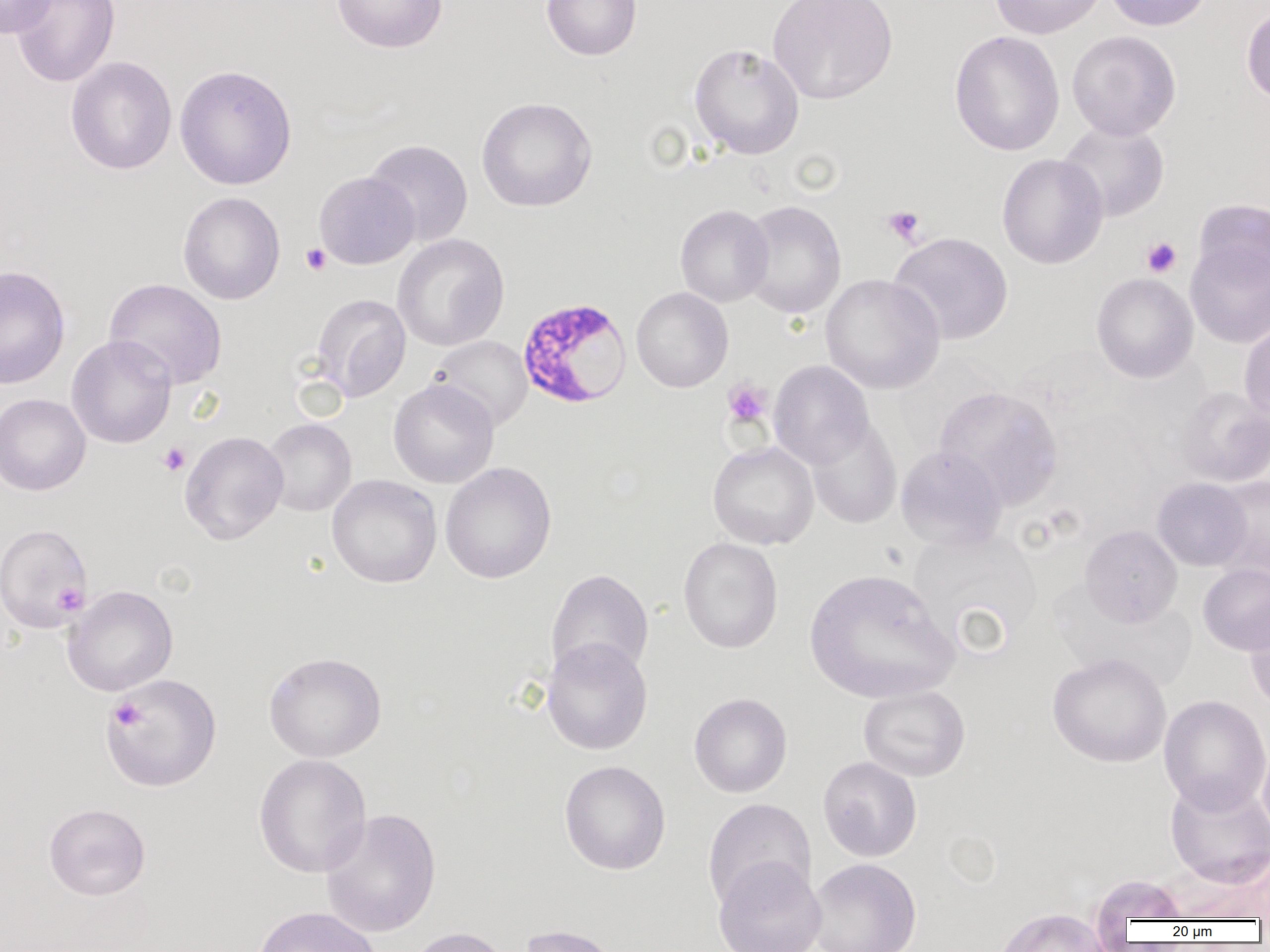 Approximate bounding boxes as [x1, y1, x2, y2] in pixels. Platelet locations: [881, 205, 926, 246], [1141, 237, 1182, 277], [300, 243, 331, 275], [722, 378, 773, 429], [157, 442, 191, 476], [53, 583, 87, 613], [109, 698, 145, 731]. Plasmodium falciparum-infected red blood cell locations: [516, 296, 632, 409]. Uninfected red blood cell locations: [1, 0, 57, 38], [10, 0, 120, 87], [332, 0, 448, 54], [541, 0, 642, 61], [768, 0, 898, 105], [991, 0, 1105, 39], [1104, 0, 1213, 31], [1241, 6, 1270, 105], [949, 30, 1065, 157], [1067, 30, 1182, 140], [689, 42, 804, 160], [65, 56, 177, 175], [174, 64, 297, 190], [476, 96, 597, 212], [1057, 121, 1170, 222], [364, 139, 473, 247], [996, 153, 1108, 269], [314, 171, 419, 270], [177, 191, 285, 305], [1192, 198, 1270, 291], [739, 200, 846, 319], [674, 204, 773, 307], [888, 231, 1013, 345], [392, 234, 509, 351], [1185, 237, 1270, 348], [0, 266, 70, 389], [1091, 272, 1198, 383], [820, 273, 946, 394], [104, 278, 227, 389], [630, 287, 733, 393], [311, 293, 411, 402], [1239, 318, 1270, 427], [67, 336, 176, 448], [430, 336, 533, 430], [768, 360, 874, 469], [388, 379, 499, 488], [933, 385, 1064, 510], [1173, 386, 1270, 487], [1, 393, 91, 496], [806, 417, 902, 529], [261, 418, 357, 516], [179, 430, 289, 545], [708, 441, 819, 549], [895, 445, 1008, 552], [440, 462, 557, 584], [327, 475, 442, 588], [1210, 476, 1270, 581], [1152, 478, 1251, 571], [0, 523, 92, 632], [1080, 525, 1182, 626], [906, 527, 1043, 657], [678, 537, 783, 653], [1198, 564, 1270, 655], [804, 568, 959, 704], [545, 569, 654, 682], [62, 585, 178, 696], [1244, 604, 1270, 711], [541, 637, 653, 756], [264, 651, 386, 762], [1047, 653, 1172, 768], [101, 674, 221, 792], [858, 685, 970, 782], [689, 693, 792, 798], [1159, 695, 1270, 814], [1257, 736, 1270, 844], [253, 753, 372, 878], [818, 756, 922, 862], [559, 760, 671, 875], [1164, 777, 1270, 887], [702, 798, 815, 911], [44, 802, 151, 900], [320, 808, 441, 938], [713, 858, 826, 952], [807, 858, 922, 952], [1089, 873, 1191, 930], [251, 906, 382, 952], [994, 907, 1113, 952], [518, 924, 623, 952], [404, 926, 516, 952]. Slide-level diagnosis: Plasmodium falciparum. Thin blood film. Image is 1270×952 pixels. Captured at 1000x magnification. Single field of view. Light microscopy.